Identify the parasite.
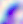
This is Toxoplasma gondii.

Summary:
  - Magnification: 400x
  - Modality: micrograph